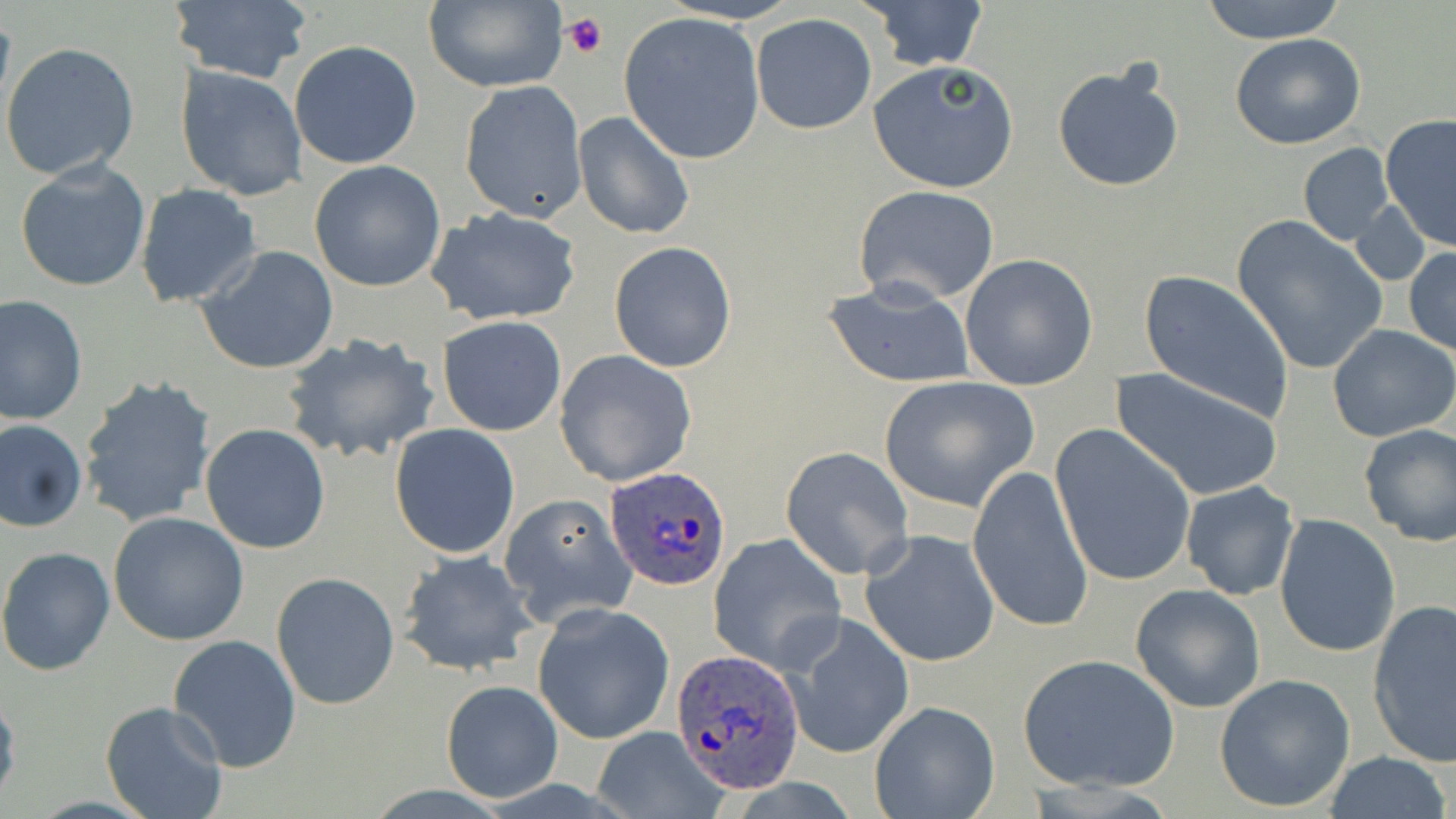
{
  "slide_level_diagnosis": "Plasmodium ovale",
  "modality": "light microscopy",
  "image_size": "1456×819 pixels",
  "plasmodium_ovale_infected_red_blood_cell_locations": "approximate bounding boxes as named x1/y1/x2/y2 corners in pixels: (x1=606, y1=467, x2=729, y2=588), (x1=670, y1=647, x2=803, y2=793)",
  "field_of_view": "one of a larger specimen",
  "platelet_locations": "approximate bounding boxes as named x1/y1/x2/y2 corners in pixels: (x1=561, y1=13, x2=608, y2=61)",
  "preparation": "thin blood smear",
  "magnification": "1000x",
  "stain": "May-Grünwald-Giemsa",
  "uninfected_red_blood_cell_locations": "approximate bounding boxes as named x1/y1/x2/y2 corners in pixels: (x1=862, y1=0, x2=990, y2=72), (x1=1196, y1=0, x2=1349, y2=45), (x1=422, y1=1, x2=567, y2=92), (x1=165, y1=2, x2=311, y2=85), (x1=619, y1=12, x2=766, y2=166), (x1=750, y1=13, x2=877, y2=135), (x1=1229, y1=33, x2=1367, y2=149), (x1=289, y1=40, x2=422, y2=169), (x1=1, y1=43, x2=141, y2=183), (x1=868, y1=60, x2=1020, y2=195), (x1=1051, y1=63, x2=1184, y2=194), (x1=175, y1=66, x2=307, y2=202), (x1=459, y1=80, x2=588, y2=223), (x1=572, y1=111, x2=695, y2=240), (x1=1378, y1=114, x2=1455, y2=251), (x1=1297, y1=142, x2=1396, y2=247), (x1=14, y1=158, x2=152, y2=294), (x1=308, y1=160, x2=446, y2=293), (x1=135, y1=183, x2=261, y2=308), (x1=854, y1=185, x2=1001, y2=305), (x1=1350, y1=201, x2=1432, y2=287), (x1=424, y1=206, x2=584, y2=327), (x1=1231, y1=216, x2=1386, y2=375), (x1=609, y1=241, x2=737, y2=374), (x1=194, y1=245, x2=340, y2=376), (x1=1404, y1=248, x2=1456, y2=356), (x1=959, y1=253, x2=1099, y2=391), (x1=1136, y1=270, x2=1295, y2=423), (x1=819, y1=274, x2=977, y2=388), (x1=0, y1=295, x2=88, y2=426), (x1=436, y1=316, x2=567, y2=435), (x1=1327, y1=324, x2=1456, y2=442), (x1=279, y1=332, x2=442, y2=467), (x1=554, y1=350, x2=697, y2=487), (x1=1110, y1=367, x2=1285, y2=501), (x1=78, y1=375, x2=216, y2=530), (x1=876, y1=375, x2=1039, y2=510), (x1=0, y1=417, x2=87, y2=532), (x1=200, y1=422, x2=331, y2=554), (x1=389, y1=423, x2=521, y2=558), (x1=1358, y1=423, x2=1456, y2=548), (x1=1051, y1=424, x2=1198, y2=588), (x1=781, y1=448, x2=914, y2=578), (x1=967, y1=464, x2=1093, y2=635), (x1=1181, y1=480, x2=1299, y2=600), (x1=499, y1=492, x2=637, y2=625), (x1=109, y1=512, x2=250, y2=647), (x1=1274, y1=513, x2=1400, y2=658), (x1=861, y1=530, x2=1000, y2=668), (x1=708, y1=534, x2=846, y2=674), (x1=0, y1=545, x2=116, y2=676), (x1=397, y1=549, x2=541, y2=678), (x1=271, y1=572, x2=401, y2=710), (x1=1130, y1=584, x2=1266, y2=713), (x1=1367, y1=600, x2=1456, y2=768), (x1=531, y1=603, x2=675, y2=745), (x1=785, y1=614, x2=914, y2=759), (x1=168, y1=633, x2=301, y2=772), (x1=1017, y1=653, x2=1180, y2=793), (x1=1214, y1=673, x2=1356, y2=812), (x1=440, y1=681, x2=563, y2=804), (x1=0, y1=691, x2=21, y2=810), (x1=868, y1=699, x2=1001, y2=818), (x1=101, y1=700, x2=229, y2=819), (x1=590, y1=727, x2=727, y2=818), (x1=1322, y1=751, x2=1453, y2=819)"
}